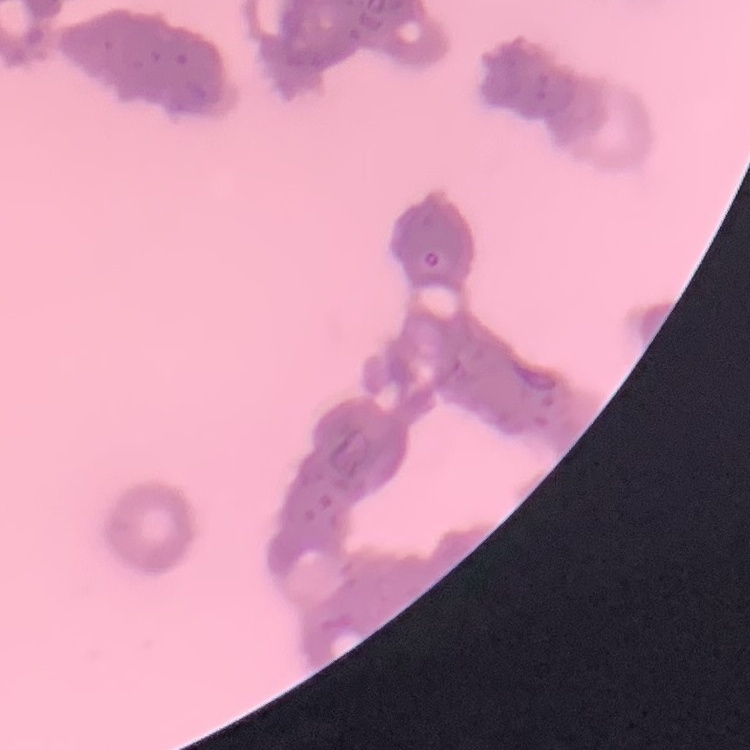
The erythrocytes exhibit rouleaux formation. Thin peripheral smear. Field's or Giemsa stain. Square crop of a larger photomicrograph.